Evaluate for malaria.
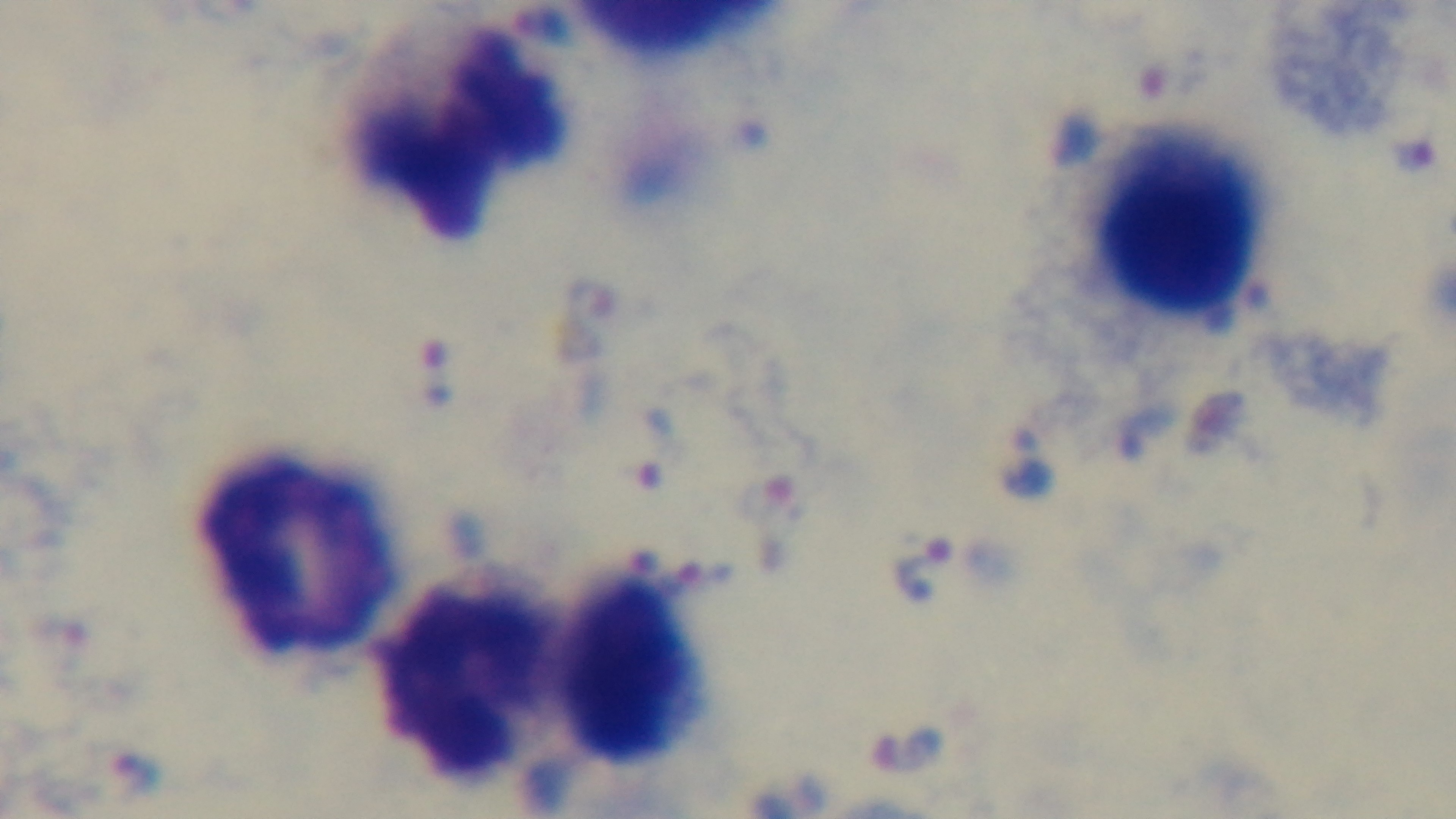
Infected.

objective = 100x oil immersion
modality = light microscopy
field of view = single
preparation = thick blood film
capture = mounted 4K digital camera
stain = Giemsa